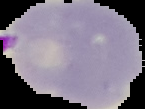

Summary:
  - Image type: segmented cell region on a black background
  - Malaria status: parasitized
  - Preparation: thin blood smear
  - Image size: 145×109 pixels